State which parasite is depicted.
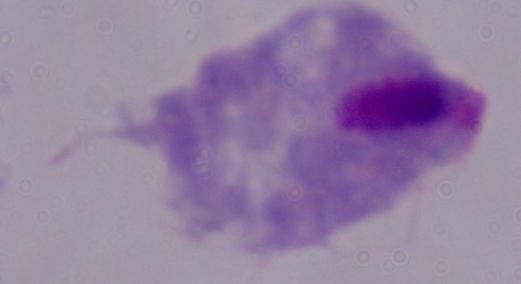
A trichomonad.

magnification = 1000x
modality = micrograph